Report the malaria status of this cell.
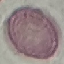

It is uninfected.

Summary:
  - Stain: Giemsa
  - Capture: smartphone camera at the microscope eyepiece
  - Image type: automatically extracted cell patch, resized to 64 × 64 pixels
  - Preparation: thin blood film